Assess the morphology of the erythrocytes.
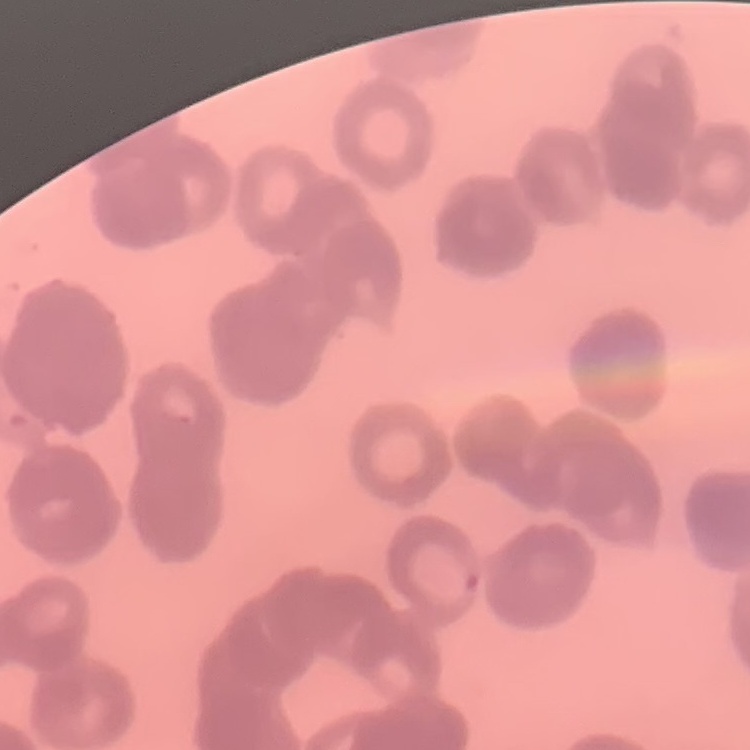

They show rouleaux formation.

Summary:
  - Preparation: thin blood film
  - Image type: one tile cut from a larger photomicrograph
  - Stain: Field's or Giemsa